Assess this cell for malaria.
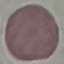
It is uninfected.

Summary:
  - Capture: smartphone camera at the microscope eyepiece
  - Preparation: thin blood film
  - Image type: automatically extracted cell patch, resized to 64 × 64 pixels
  - Stain: Giemsa